Locate and identify every blood parasite.
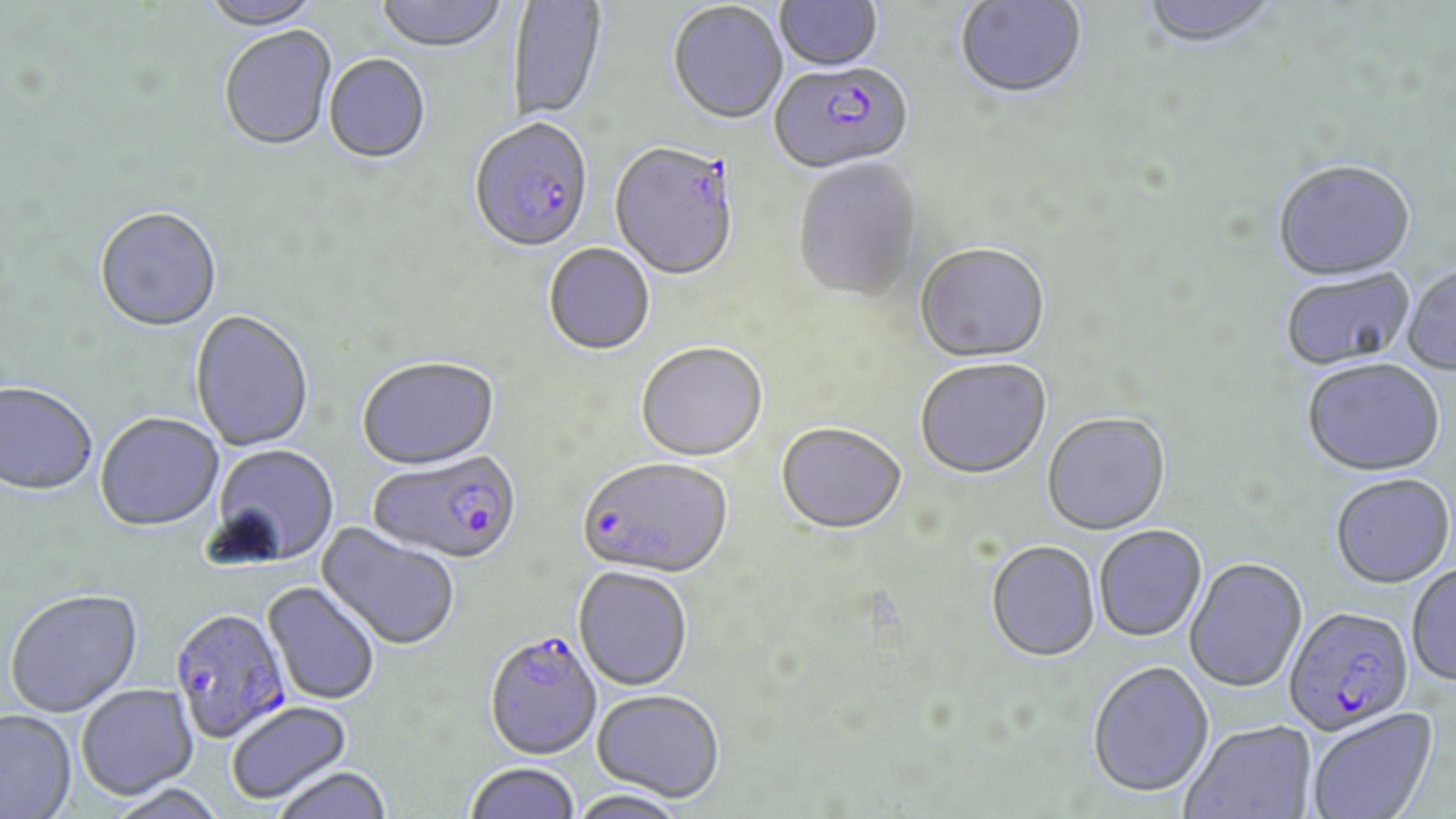

Approximate bounding boxes as (x1, y1, x2, y2) in pixels.
Plasmodium falciparum-infected red blood cells: (767, 64, 912, 179), (469, 121, 594, 256), (609, 144, 739, 283), (368, 452, 522, 567), (576, 458, 732, 582), (1283, 607, 1415, 738), (169, 609, 291, 745), (483, 632, 602, 760).
No Plasmodium ovale, Plasmodium malariae, Plasmodium vivax, Babesia divergens, or Trypanosoma brucei observed.

{
  "slide_level_diagnosis": "Plasmodium falciparum",
  "image_size": "1456×819 pixels",
  "field_of_view": "one of a larger specimen",
  "preparation": "thin blood film",
  "magnification": "1000x",
  "modality": "optical microscopy",
  "stain": "May-Grünwald-Giemsa",
  "uninfected_red_blood_cell_locations": "approximate bounding boxes as (x1, y1, x2, y2) in pixels: (202, 0, 323, 32), (376, 0, 507, 55), (775, 0, 883, 74), (954, 0, 1088, 102), (1138, 0, 1280, 51), (508, 1, 607, 123), (668, 3, 788, 126), (219, 27, 337, 153), (324, 55, 431, 165), (793, 159, 923, 304), (1272, 162, 1417, 285), (94, 210, 222, 334), (544, 244, 655, 357), (915, 245, 1050, 365), (1402, 265, 1456, 377), (1281, 269, 1416, 373), (190, 311, 314, 452), (636, 344, 767, 463), (357, 358, 501, 473), (915, 359, 1052, 481), (1302, 362, 1445, 479), (0, 385, 97, 497), (95, 414, 224, 534), (1042, 414, 1171, 537), (775, 423, 907, 536), (208, 444, 340, 569), (1331, 475, 1455, 590), (317, 521, 461, 653), (1094, 526, 1206, 643), (986, 542, 1100, 663), (1184, 559, 1307, 694), (1407, 564, 1456, 686), (573, 567, 693, 691), (263, 582, 380, 706), (5, 590, 144, 719), (1087, 662, 1214, 800), (76, 685, 199, 802), (592, 689, 725, 802), (226, 701, 353, 805), (1306, 709, 1438, 819), (0, 711, 77, 818), (1182, 722, 1317, 819), (464, 762, 580, 819), (272, 767, 393, 819), (106, 785, 228, 819), (569, 788, 690, 819)"
}